Assess for malaria.
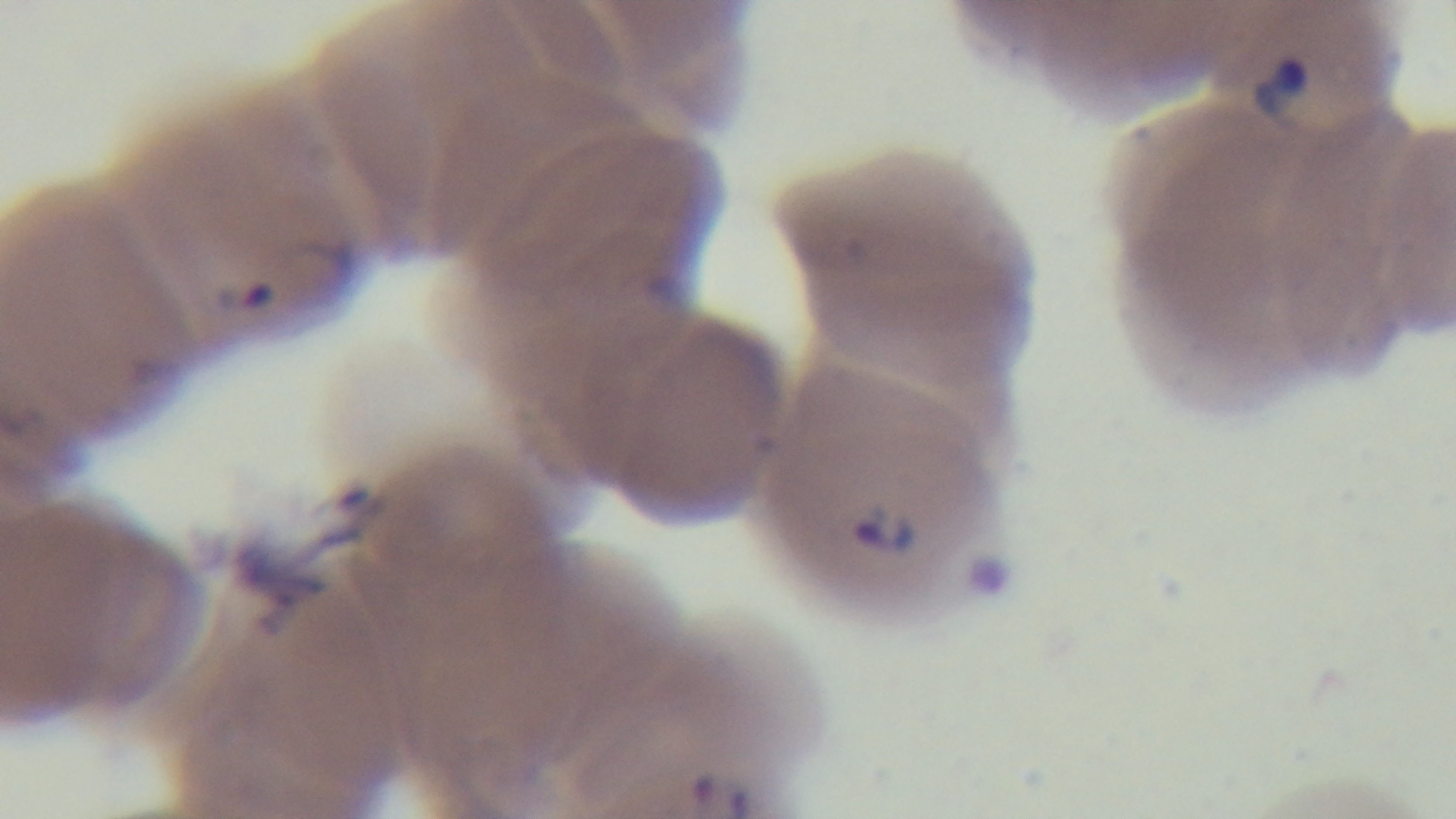
Infected.

Summary:
  - Objective: 100x oil immersion
  - Modality: light microscopy
  - Capture: mounted 4K digital camera
  - Stain: Giemsa
  - Field of view: single
  - Preparation: thin blood film